Report the malaria status of this cell.
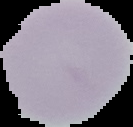
It is uninfected.

image_size: 133×127 pixels
preparation: thin blood film
image_type: cell region segmented out of the field of view; surrounding area masked to black